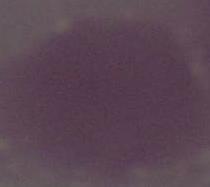
Micrograph. An erythrocyte is shown. Captured at 1000x magnification.